Give the position of every Plasmodium parasite visible.
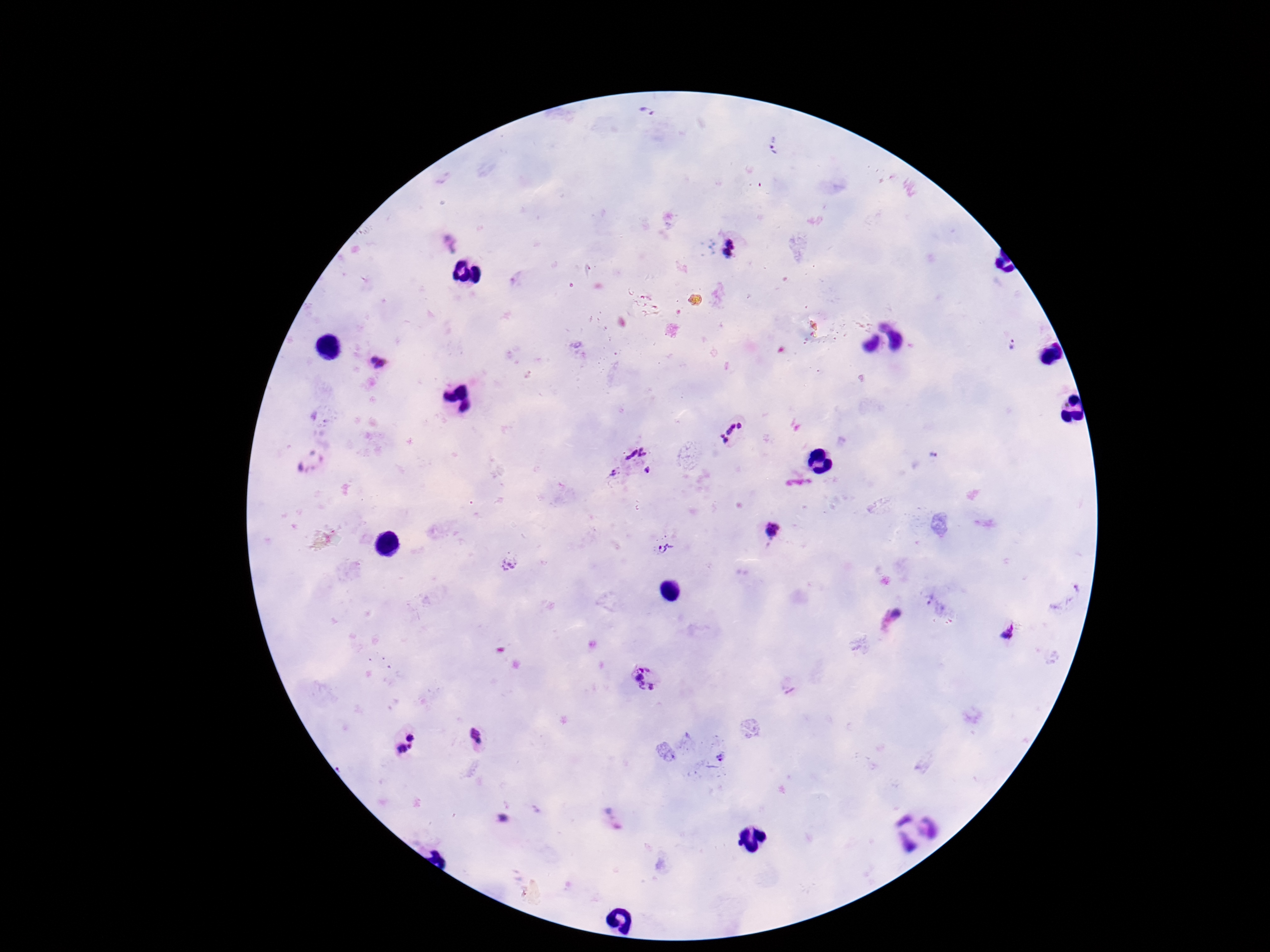
Approximate centers as [x, y] in pixels.
Plasmodium parasites: [653, 114], [775, 148], [449, 244], [728, 246], [1010, 344], [372, 366], [732, 432], [636, 452], [935, 456], [647, 471], [614, 472], [773, 530], [668, 547], [509, 562], [896, 614], [1005, 635], [643, 678], [476, 738], [404, 740], [719, 757], [499, 820].

Patient malaria status: positive. One field from this slide. Image is 1270×952 pixels. Smartphone photograph taken through the microscope eyepiece. Giemsa-stained preparation. 100x magnification. Thick blood film.